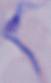 A trypanosome is shown. Photomicrograph. 1000x magnification.